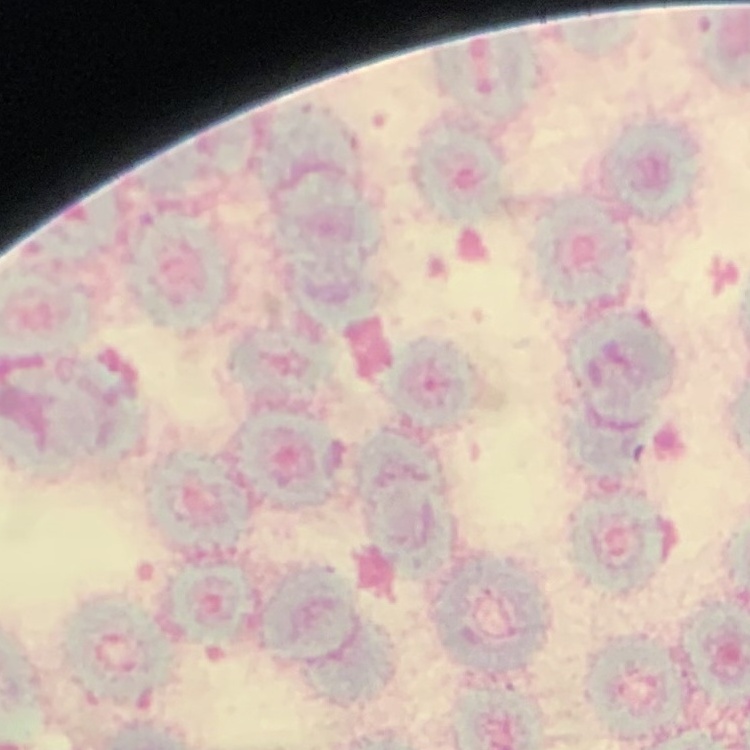

Summary:
  - Red blood cell morphology: rouleaux formation
  - Preparation: thin peripheral smear
  - Image type: square crop of a larger photomicrograph
  - Stain: Field's or Giemsa